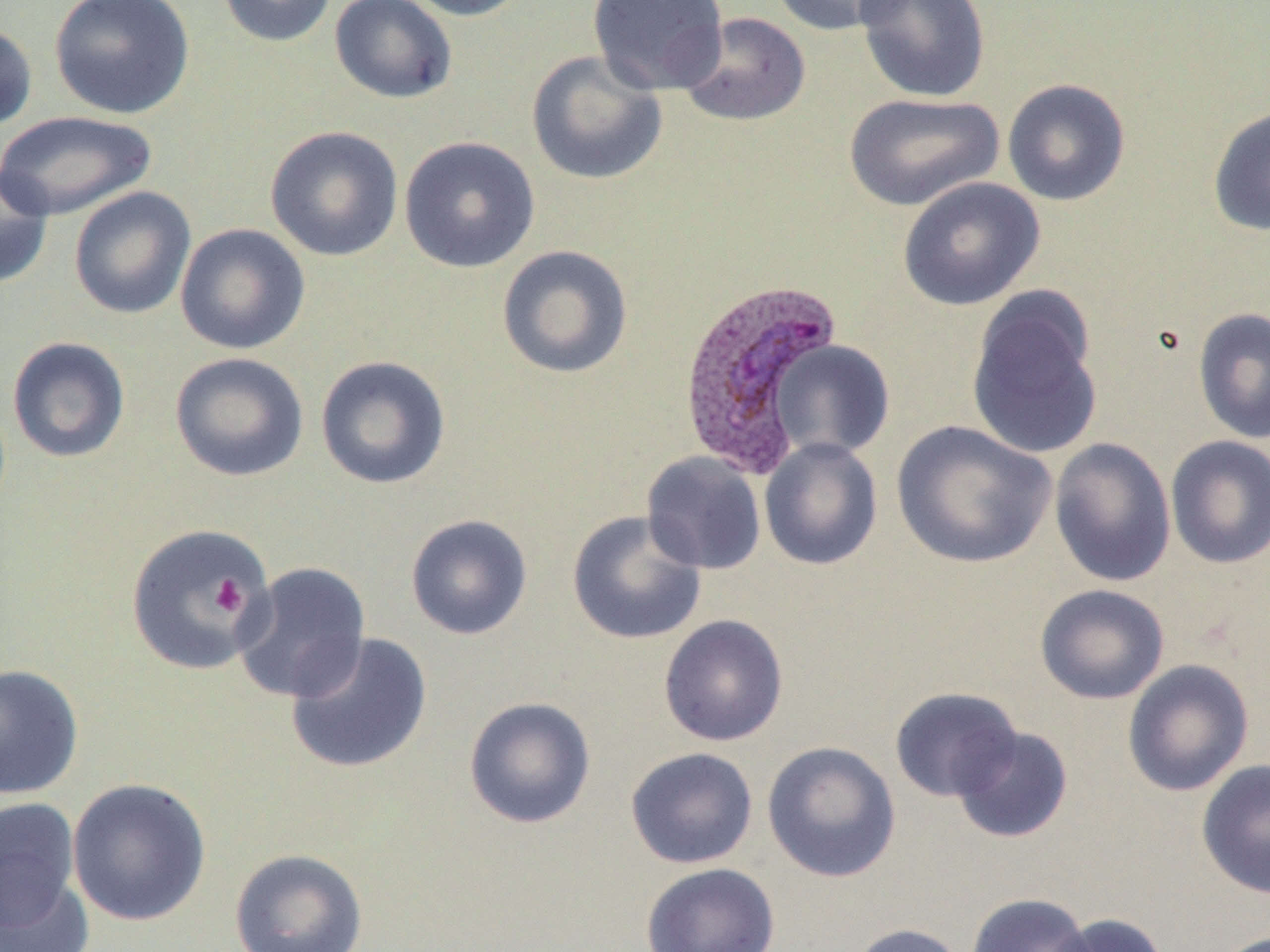

Summary:
  - Coordinate format: approximate bounding boxes as [x1, y1, x2, y2] in pixels
  - Plasmodium vivax-infected red blood cell locations: [676, 277, 843, 478]
  - Platelet locations: [211, 576, 248, 616]
  - Uninfected red blood cell locations: [49, 0, 195, 119], [215, 0, 339, 48], [329, 0, 458, 105], [399, 0, 533, 21], [587, 0, 729, 95], [770, 0, 911, 37], [855, 0, 991, 104], [678, 11, 812, 128], [0, 21, 37, 132], [526, 50, 668, 185], [1002, 78, 1131, 206], [843, 92, 1005, 212], [1207, 104, 1270, 237], [0, 110, 159, 221], [264, 125, 404, 262], [399, 136, 540, 273], [0, 160, 53, 290], [897, 176, 1045, 311], [69, 186, 196, 320], [175, 223, 311, 355], [496, 245, 634, 379], [966, 288, 1104, 461], [1193, 307, 1270, 444], [6, 336, 131, 463], [770, 340, 895, 460], [169, 352, 309, 482], [315, 355, 452, 489], [891, 420, 1056, 569], [1165, 435, 1270, 570], [759, 437, 883, 570], [1049, 437, 1177, 587], [640, 452, 767, 574], [567, 510, 708, 646], [405, 513, 533, 640], [125, 524, 274, 676], [231, 561, 372, 703], [1034, 584, 1170, 704], [658, 614, 789, 747], [285, 631, 433, 775], [1122, 659, 1254, 797], [0, 663, 84, 800], [890, 686, 1023, 803], [463, 696, 596, 829], [951, 726, 1074, 843], [762, 740, 902, 882], [625, 746, 759, 869], [1196, 759, 1270, 899], [67, 777, 212, 926], [0, 798, 81, 931], [229, 848, 369, 952], [641, 862, 780, 952], [0, 872, 94, 952], [966, 892, 1094, 952], [1049, 913, 1170, 952], [846, 922, 967, 952]
  - Slide-level diagnosis: Plasmodium vivax
  - Image size: 1270×952 pixels
  - Preparation: thin blood smear
  - Field of view: single
  - Magnification: 1000x
  - Modality: light microscopy